Evaluate for Plasmodium parasites.
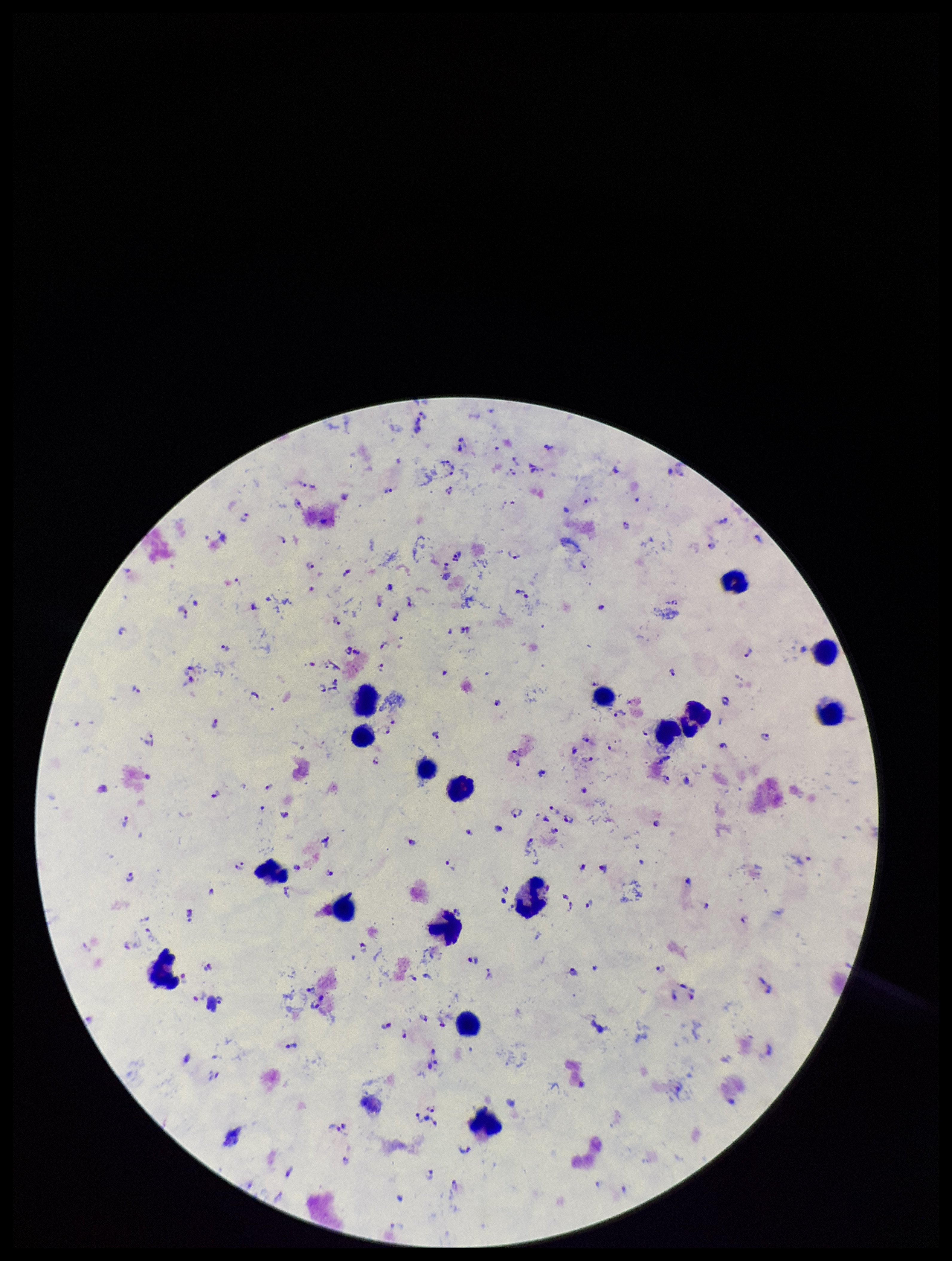
Seen.

leukocyte count = 17
image size = 952×1261 pixels
patient malaria status = positive
species reported for this patient = Plasmodium falciparum
stain = Giemsa
capture = smartphone photograph through the microscope eyepiece
field of view = single
preparation = thick blood smear
parasite count = 130